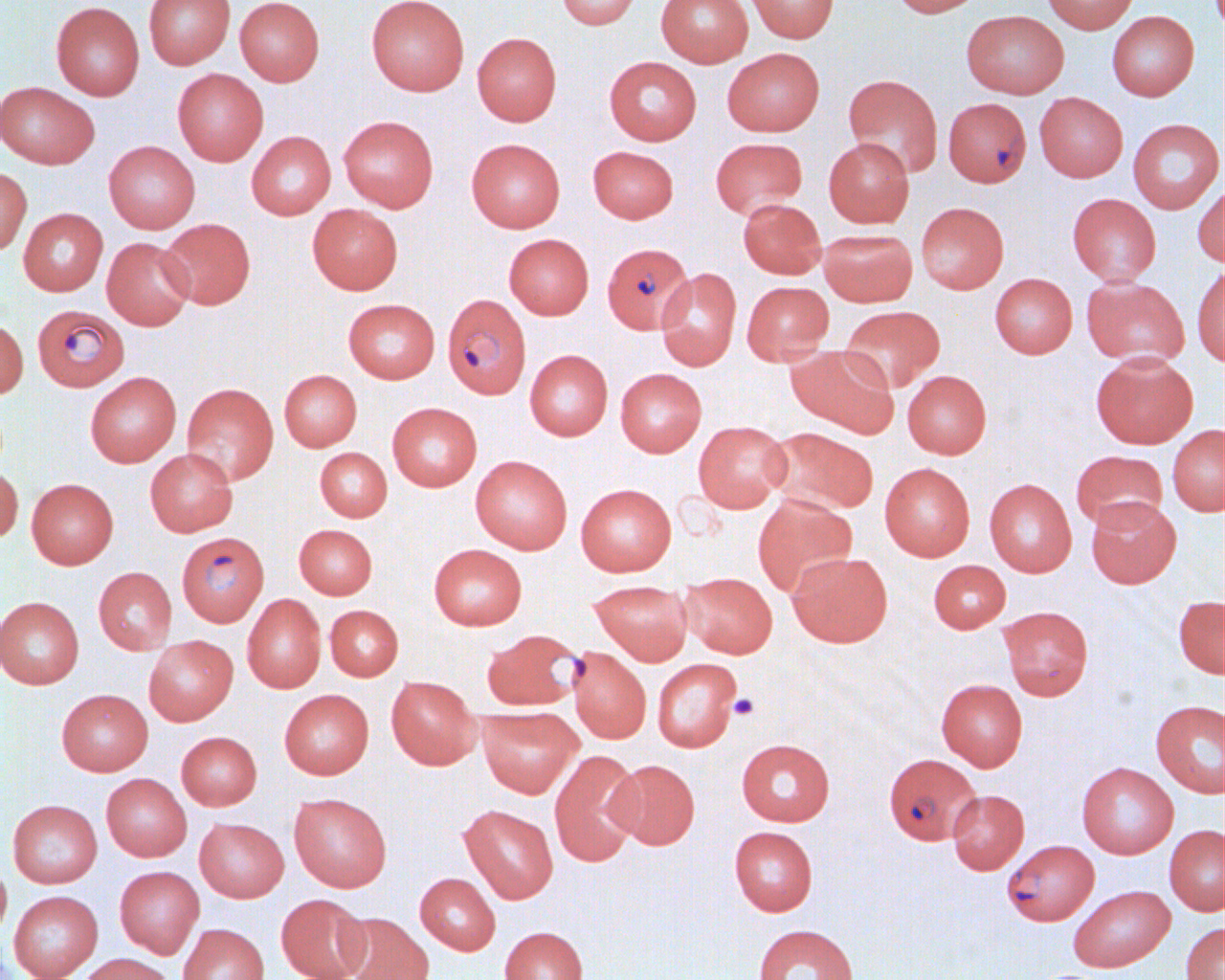
slide-level diagnosis = Plasmodium falciparum
field of view = single
modality = light microscopy
magnification = 1000x
preparation = thin blood film
Plasmodium falciparum-infected red blood cell locations = approximate bounding boxes as (x1,y1)-(x2,y2) corner pairs in pixels: (948,105)-(1037,195), (602,243)-(697,334), (443,294)-(531,398), (31,304)-(130,392), (176,531)-(269,627), (480,629)-(585,712), (883,753)-(981,845), (1002,839)-(1099,926)
uninfected red blood cell locations = approximate bounding boxes as (x1,y1)-(x2,y2) corner pairs in pixels: (143,0)-(235,69), (234,0)-(324,86), (366,0)-(469,96), (557,0)-(641,29), (656,0)-(753,67), (746,0)-(839,43), (891,0)-(983,17), (1041,0)-(1138,33), (50,2)-(145,100), (962,10)-(1069,98), (1106,10)-(1200,101), (472,32)-(562,126), (722,47)-(825,136), (604,56)-(701,145), (172,68)-(268,165), (843,74)-(942,176), (0,81)-(99,169), (1034,92)-(1128,182), (338,115)-(438,212), (1128,118)-(1223,214), (246,131)-(336,220), (823,136)-(914,228), (710,137)-(807,218), (466,138)-(566,232), (103,140)-(200,233), (587,146)-(679,223), (0,166)-(32,256), (1194,180)-(1224,269), (1067,193)-(1161,285), (738,198)-(826,279), (915,202)-(1009,294), (307,204)-(403,294), (18,208)-(108,296), (158,218)-(255,310), (818,229)-(918,307), (503,233)-(594,319), (101,237)-(195,330), (1193,265)-(1224,368), (655,268)-(741,371), (990,273)-(1077,358), (1081,276)-(1190,368), (741,281)-(834,363), (342,298)-(440,383), (839,305)-(945,393), (0,318)-(28,399), (786,345)-(899,437), (525,349)-(613,441), (1090,351)-(1198,448), (615,368)-(707,457), (279,370)-(362,451), (902,370)-(991,458), (85,372)-(181,467), (182,383)-(278,485), (387,402)-(482,491), (693,420)-(791,512), (1167,424)-(1225,516), (765,427)-(879,516), (315,447)-(392,522), (145,448)-(238,537), (1070,450)-(1168,531), (470,456)-(572,554), (879,462)-(975,561), (0,465)-(23,545), (26,478)-(118,569), (984,478)-(1076,577), (575,483)-(676,576), (752,494)-(857,596), (1086,495)-(1181,588), (294,524)-(377,599), (428,543)-(527,630), (786,551)-(893,647), (928,559)-(1011,633), (93,566)-(176,655), (681,572)-(777,658), (589,580)-(692,665), (242,594)-(326,693), (1173,595)-(1225,678), (0,596)-(84,689), (324,604)-(403,681), (998,605)-(1094,701), (144,635)-(238,726), (567,647)-(651,743), (652,658)-(740,752), (386,676)-(481,770), (936,678)-(1028,771), (56,688)-(153,776), (279,689)-(374,779), (1150,700)-(1225,798), (477,707)-(582,798), (176,731)-(261,810), (735,738)-(835,826), (549,750)-(644,867), (608,759)-(700,849), (1076,762)-(1178,859), (101,773)-(192,861), (947,789)-(1029,875), (288,792)-(392,892), (7,799)-(102,888), (459,804)-(559,904), (194,817)-(289,902), (1164,824)-(1225,916), (729,826)-(818,916), (0,860)-(12,942), (114,866)-(204,958), (415,872)-(500,955), (1068,885)-(1175,972), (8,890)-(103,980), (276,894)-(370,980), (339,913)-(433,980), (1181,921)-(1225,980), (178,923)-(269,980), (754,924)-(859,980), (499,926)-(588,980), (75,953)-(176,980)
image size = 1225×980 pixels
platelet locations = approximate bounding boxes as (x1,y1)-(x2,y2) corner pairs in pixels: (728,693)-(759,720)